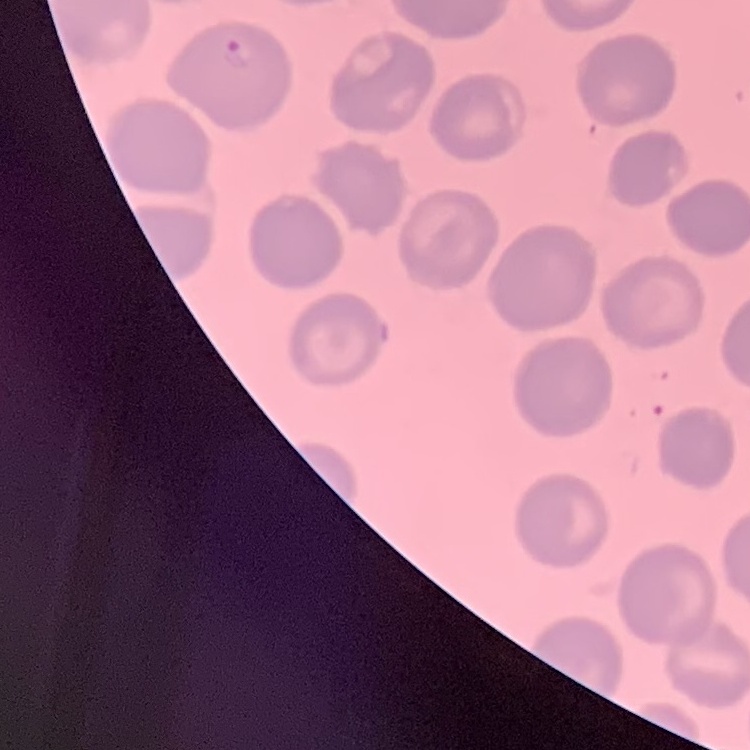
{
  "red_blood_cell_morphology": "no rouleaux formation",
  "image_type": "square crop of a larger photomicrograph",
  "preparation": "thin blood film",
  "stain": "Field's or Giemsa"
}